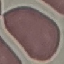

result = no malaria parasites seen
image type = cell patch, automatically extracted from a larger field of view and resized to 64 × 64 pixels
stain = Giemsa
preparation = thin blood smear
capture = smartphone through the microscope eyepiece